Name the blood parasite species.
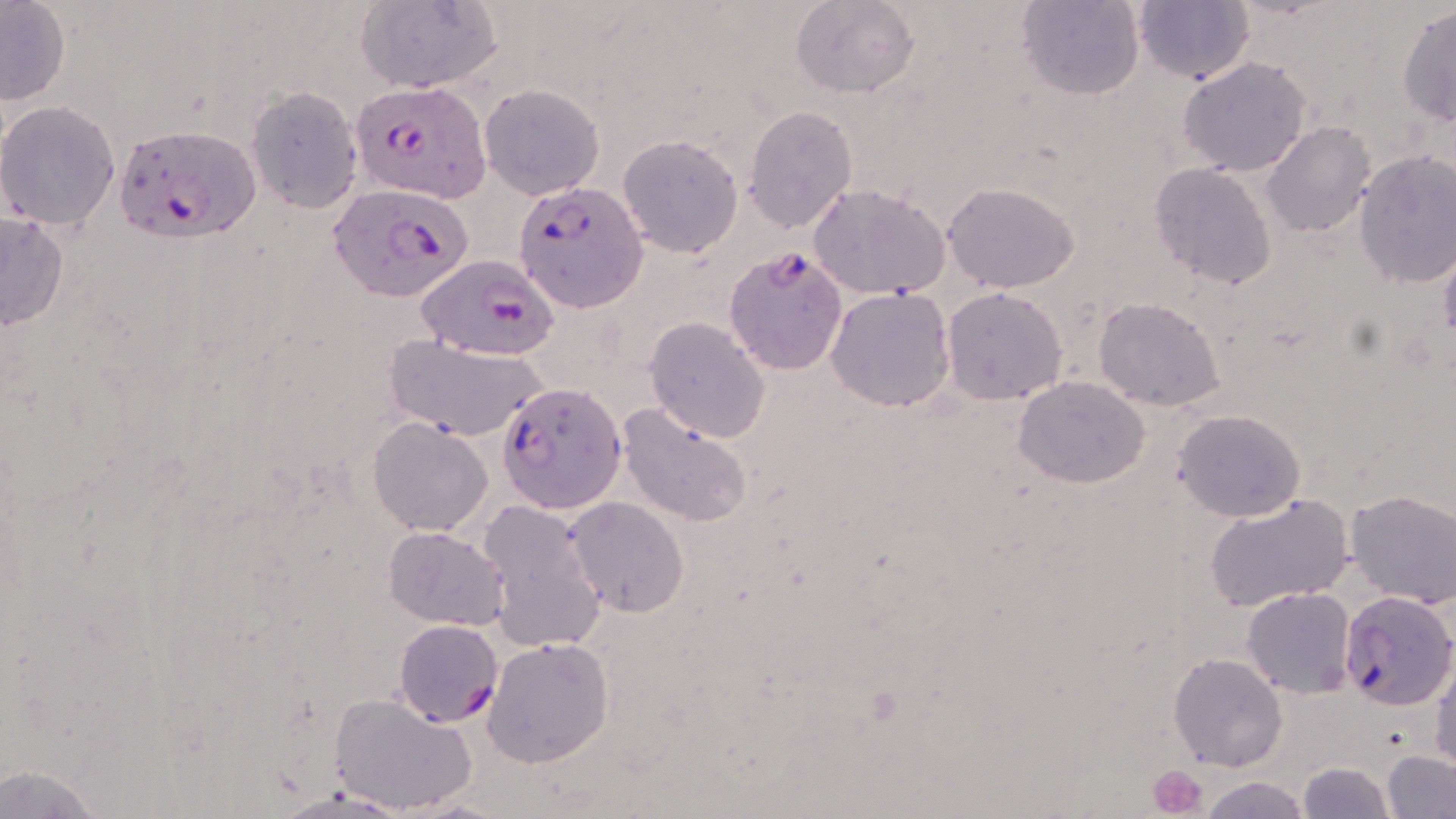

Plasmodium falciparum.

uninfected red blood cell locations = approximate bounding boxes as named x1/y1/x2/y2 corners in pixels: (x1=0, y1=0, x2=70, y2=107), (x1=354, y1=0, x2=502, y2=94), (x1=790, y1=0, x2=918, y2=100), (x1=1016, y1=0, x2=1145, y2=101), (x1=1133, y1=0, x2=1254, y2=85), (x1=1397, y1=5, x2=1455, y2=127), (x1=1176, y1=55, x2=1314, y2=176), (x1=479, y1=83, x2=605, y2=200), (x1=244, y1=86, x2=364, y2=213), (x1=0, y1=101, x2=119, y2=232), (x1=742, y1=104, x2=858, y2=232), (x1=1261, y1=121, x2=1378, y2=237), (x1=616, y1=134, x2=744, y2=258), (x1=1352, y1=150, x2=1456, y2=287), (x1=1147, y1=162, x2=1278, y2=289), (x1=807, y1=181, x2=949, y2=301), (x1=942, y1=183, x2=1080, y2=294), (x1=0, y1=212, x2=70, y2=332), (x1=1439, y1=241, x2=1456, y2=350), (x1=825, y1=286, x2=956, y2=413), (x1=942, y1=286, x2=1070, y2=405), (x1=1093, y1=296, x2=1226, y2=410), (x1=643, y1=316, x2=770, y2=442), (x1=383, y1=337, x2=547, y2=442), (x1=1013, y1=376, x2=1151, y2=489), (x1=617, y1=403, x2=753, y2=530), (x1=1172, y1=408, x2=1306, y2=523), (x1=368, y1=417, x2=494, y2=536), (x1=1344, y1=490, x2=1456, y2=608), (x1=1203, y1=492, x2=1354, y2=613), (x1=565, y1=496, x2=691, y2=618), (x1=477, y1=498, x2=609, y2=655), (x1=383, y1=526, x2=509, y2=630), (x1=1241, y1=586, x2=1358, y2=697), (x1=483, y1=636, x2=613, y2=767), (x1=1167, y1=652, x2=1287, y2=772), (x1=1430, y1=654, x2=1455, y2=771), (x1=328, y1=692, x2=478, y2=815), (x1=1381, y1=749, x2=1456, y2=819), (x1=1298, y1=761, x2=1393, y2=818), (x1=1, y1=764, x2=110, y2=818), (x1=1199, y1=776, x2=1311, y2=819), (x1=396, y1=795, x2=510, y2=819)
platelet locations = approximate bounding boxes as named x1/y1/x2/y2 corners in pixels: (x1=1150, y1=763, x2=1208, y2=816)
magnification = 1000x
stain = May-Grünwald-Giemsa
Plasmodium falciparum-infected red blood cell locations = approximate bounding boxes as named x1/y1/x2/y2 corners in pixels: (x1=352, y1=79, x2=492, y2=203), (x1=112, y1=121, x2=263, y2=243), (x1=513, y1=179, x2=648, y2=314), (x1=329, y1=184, x2=476, y2=303), (x1=723, y1=246, x2=848, y2=378), (x1=416, y1=256, x2=557, y2=362), (x1=501, y1=382, x2=626, y2=512), (x1=1337, y1=591, x2=1455, y2=709), (x1=393, y1=619, x2=503, y2=725)
image size = 1456×819 pixels
field of view = one of a larger specimen
preparation = thin blood smear
modality = optical microscopy